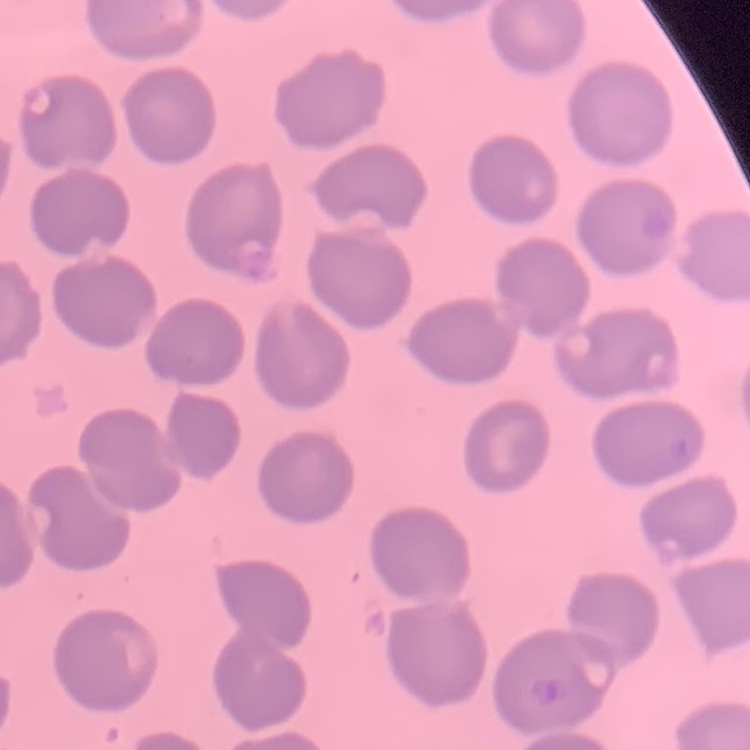
Summary:
  - Red blood cell morphology: no rouleaux formation
  - Stain: Field's or Giemsa
  - Image type: one tile cut from a larger photomicrograph
  - Preparation: thin blood film